Locate every blood parasite and identify its species.
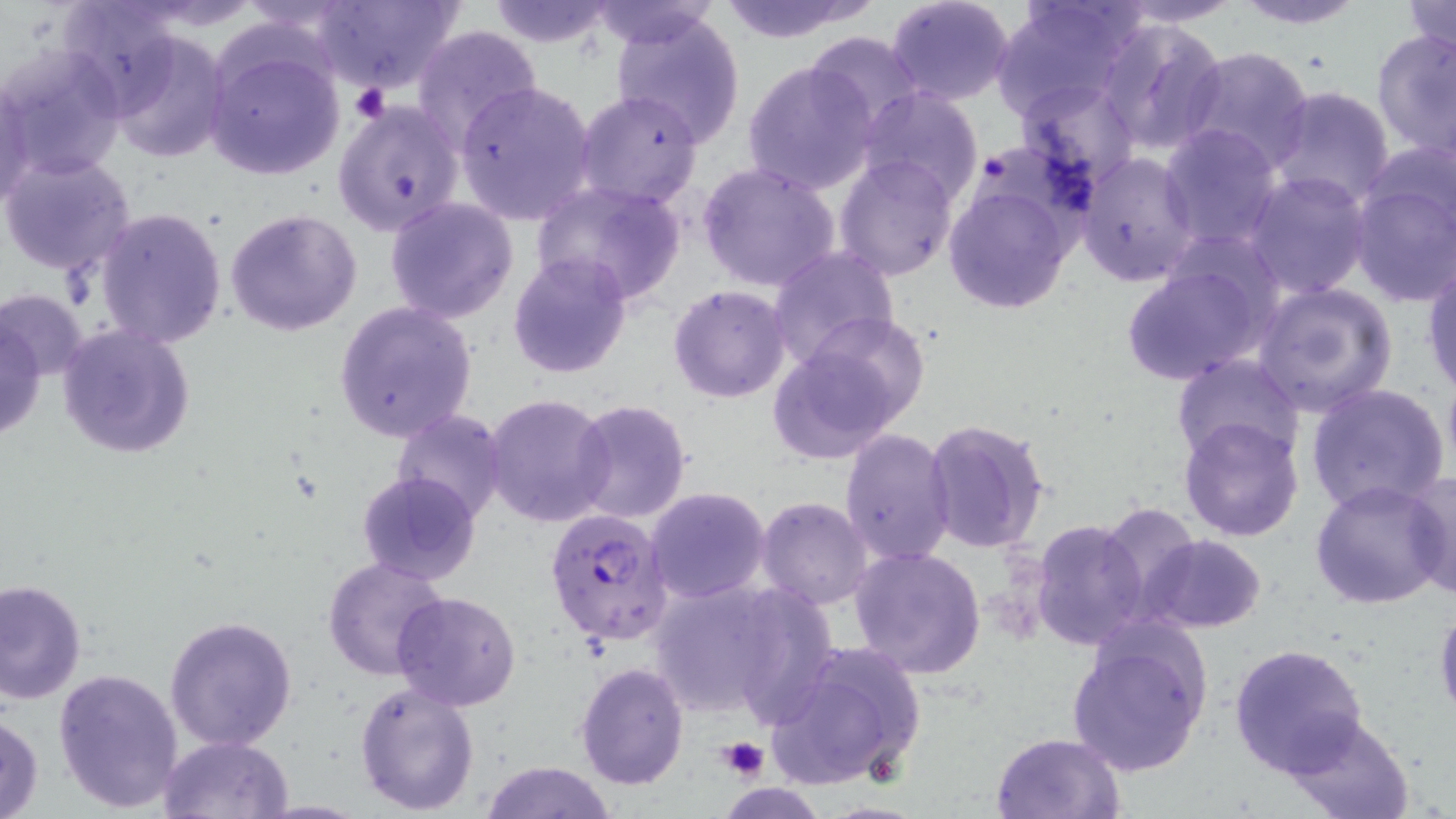
Approximate bounding boxes as named x1/y1/x2/y2 corners in pixels.
Plasmodium falciparum-infected red blood cells: (x1=545, y1=506, x2=673, y2=647).
No Plasmodium ovale, Plasmodium malariae, Plasmodium vivax, Babesia divergens, or Trypanosoma brucei observed.

Uninfected red blood cell locations: (x1=56, y1=0, x2=185, y2=116), (x1=313, y1=0, x2=464, y2=94), (x1=714, y1=0, x2=877, y2=44), (x1=886, y1=0, x2=1017, y2=106), (x1=992, y1=0, x2=1147, y2=122), (x1=1111, y1=0, x2=1247, y2=27), (x1=1230, y1=0, x2=1368, y2=29), (x1=482, y1=1, x2=620, y2=50), (x1=589, y1=2, x2=720, y2=49), (x1=1400, y1=2, x2=1456, y2=62), (x1=608, y1=8, x2=747, y2=147), (x1=1096, y1=17, x2=1229, y2=157), (x1=410, y1=25, x2=544, y2=153), (x1=1371, y1=26, x2=1455, y2=161), (x1=802, y1=30, x2=925, y2=136), (x1=107, y1=31, x2=232, y2=162), (x1=205, y1=40, x2=345, y2=181), (x1=1, y1=46, x2=126, y2=183), (x1=1180, y1=46, x2=1316, y2=173), (x1=742, y1=59, x2=879, y2=196), (x1=1016, y1=77, x2=1141, y2=192), (x1=0, y1=80, x2=37, y2=209), (x1=454, y1=80, x2=597, y2=226), (x1=1268, y1=86, x2=1397, y2=208), (x1=856, y1=88, x2=983, y2=206), (x1=576, y1=89, x2=704, y2=210), (x1=334, y1=99, x2=463, y2=236), (x1=1158, y1=125, x2=1283, y2=252), (x1=1361, y1=138, x2=1456, y2=247), (x1=1076, y1=151, x2=1199, y2=287), (x1=0, y1=152, x2=137, y2=279), (x1=835, y1=152, x2=959, y2=280), (x1=696, y1=160, x2=843, y2=293), (x1=1242, y1=170, x2=1373, y2=300), (x1=1348, y1=174, x2=1456, y2=308), (x1=531, y1=179, x2=688, y2=305), (x1=940, y1=180, x2=1080, y2=315), (x1=385, y1=199, x2=519, y2=323), (x1=95, y1=206, x2=227, y2=349), (x1=226, y1=208, x2=364, y2=336), (x1=766, y1=246, x2=899, y2=372), (x1=506, y1=251, x2=633, y2=378), (x1=1119, y1=252, x2=1282, y2=387), (x1=1422, y1=255, x2=1456, y2=398), (x1=1251, y1=282, x2=1399, y2=417), (x1=669, y1=285, x2=791, y2=402), (x1=1, y1=289, x2=90, y2=384), (x1=332, y1=300, x2=479, y2=443), (x1=1, y1=317, x2=47, y2=442), (x1=58, y1=324, x2=195, y2=459), (x1=767, y1=328, x2=915, y2=464), (x1=1171, y1=355, x2=1303, y2=466), (x1=1304, y1=382, x2=1450, y2=516), (x1=483, y1=392, x2=613, y2=528), (x1=567, y1=398, x2=692, y2=523), (x1=390, y1=409, x2=509, y2=525), (x1=1178, y1=416, x2=1306, y2=541), (x1=923, y1=418, x2=1050, y2=554), (x1=840, y1=428, x2=958, y2=565), (x1=354, y1=470, x2=481, y2=587), (x1=1404, y1=470, x2=1456, y2=600), (x1=1310, y1=479, x2=1451, y2=611), (x1=645, y1=487, x2=771, y2=604), (x1=756, y1=496, x2=874, y2=608), (x1=1098, y1=504, x2=1205, y2=623), (x1=1029, y1=517, x2=1148, y2=651), (x1=1141, y1=534, x2=1267, y2=633), (x1=848, y1=547, x2=987, y2=681), (x1=323, y1=556, x2=450, y2=681), (x1=0, y1=578, x2=86, y2=707), (x1=644, y1=578, x2=801, y2=719), (x1=392, y1=591, x2=521, y2=710), (x1=1434, y1=603, x2=1456, y2=726), (x1=165, y1=615, x2=296, y2=752), (x1=1066, y1=627, x2=1210, y2=778), (x1=766, y1=640, x2=926, y2=791), (x1=1229, y1=642, x2=1370, y2=777), (x1=574, y1=661, x2=689, y2=791), (x1=52, y1=667, x2=185, y2=814), (x1=354, y1=678, x2=481, y2=814), (x1=1, y1=710, x2=45, y2=819), (x1=1279, y1=712, x2=1419, y2=819), (x1=990, y1=731, x2=1126, y2=819), (x1=160, y1=735, x2=294, y2=819), (x1=480, y1=762, x2=617, y2=819). Platelet locations: (x1=350, y1=83, x2=388, y2=124), (x1=717, y1=736, x2=769, y2=780). Slide-level diagnosis: Plasmodium falciparum. Thin blood film. 1000x magnification. Image is 1456×819 pixels. Light microscopy. May-Grünwald-Giemsa-stained preparation. One field of a larger specimen.